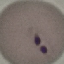
Summary:
  - Malaria status: parasitized
  - Image type: cell patch, automatically extracted from a larger field of view and resized to 64 × 64 pixels
  - Capture: smartphone through the microscope eyepiece
  - Preparation: thin smear
  - Stain: Giemsa